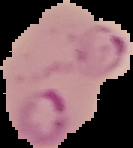

result = Plasmodium parasites identified
image size = 133×148 pixels
image type = segmented cell region on a black background
preparation = thin blood film